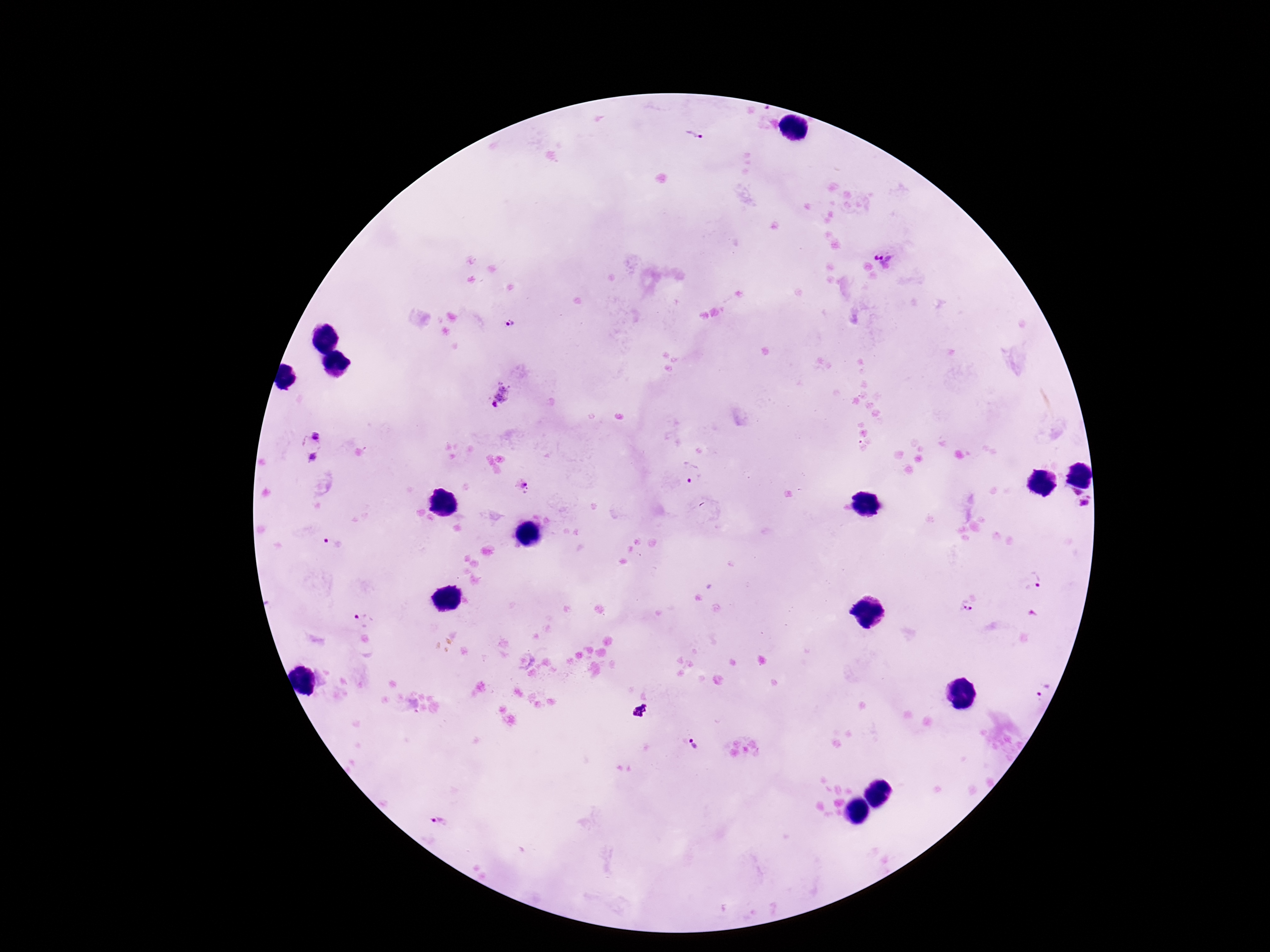

Approximate object centers, in pixels from the top-left corner.
Summary:
  - Plasmodium parasite locations: (x=695, y=135), (x=884, y=260), (x=511, y=324), (x=499, y=397), (x=315, y=434), (x=313, y=456), (x=691, y=474), (x=523, y=487), (x=1075, y=491), (x=1085, y=504), (x=332, y=542), (x=1035, y=580), (x=965, y=608), (x=365, y=620), (x=1044, y=691), (x=640, y=711), (x=693, y=745), (x=443, y=820)
  - Field of view: one from this slide
  - Preparation: thick blood film
  - Capture: smartphone camera through the microscope eyepiece
  - Stain: Giemsa
  - Magnification: 100x
  - Image size: 1270×952 pixels
  - Patient malaria status: infected